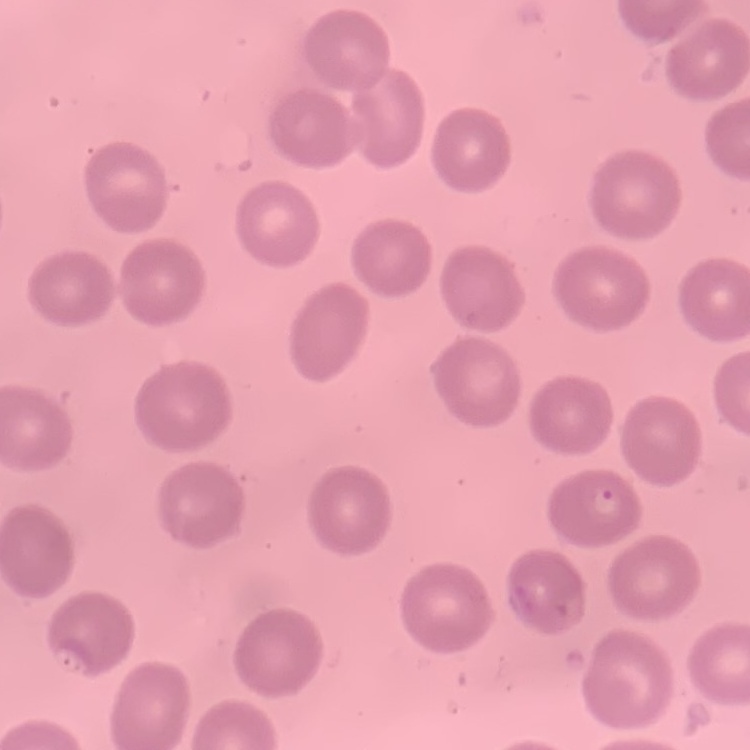

red blood cell morphology = no rouleaux formation
preparation = thin peripheral smear
image type = square crop of a larger photomicrograph
stain = Field's or Giemsa